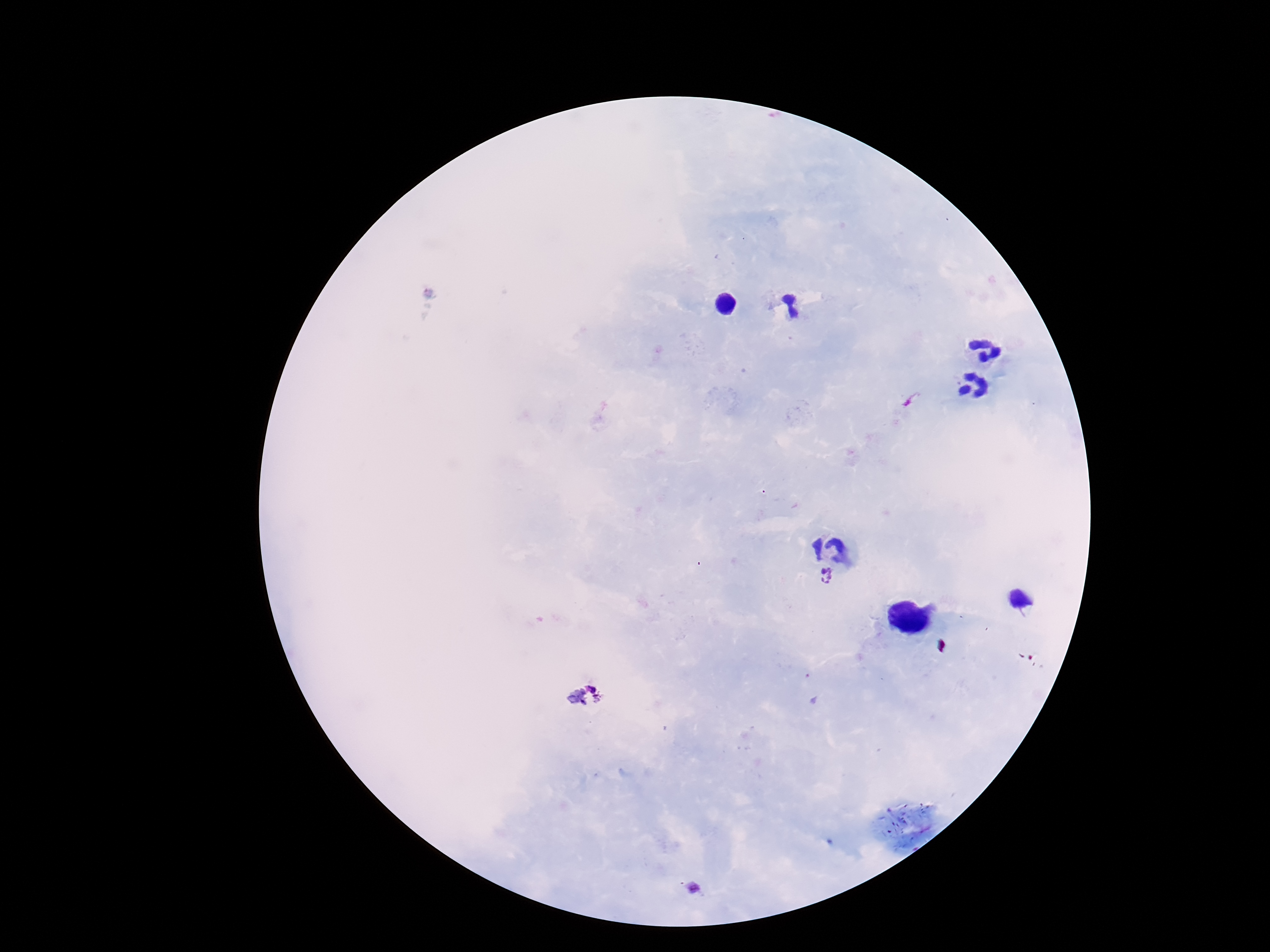

Approximate centers as {x, y} in pixels.
Summary:
  - Plasmodium parasite locations: {826, 579}, {584, 697}
  - Image size: 1270×952 pixels
  - Patient malaria status: infected
  - Magnification: 100x
  - Stain: Giemsa
  - Capture: smartphone camera through the microscope eyepiece
  - Preparation: thick blood smear
  - Field of view: single